Mark where platelets are.
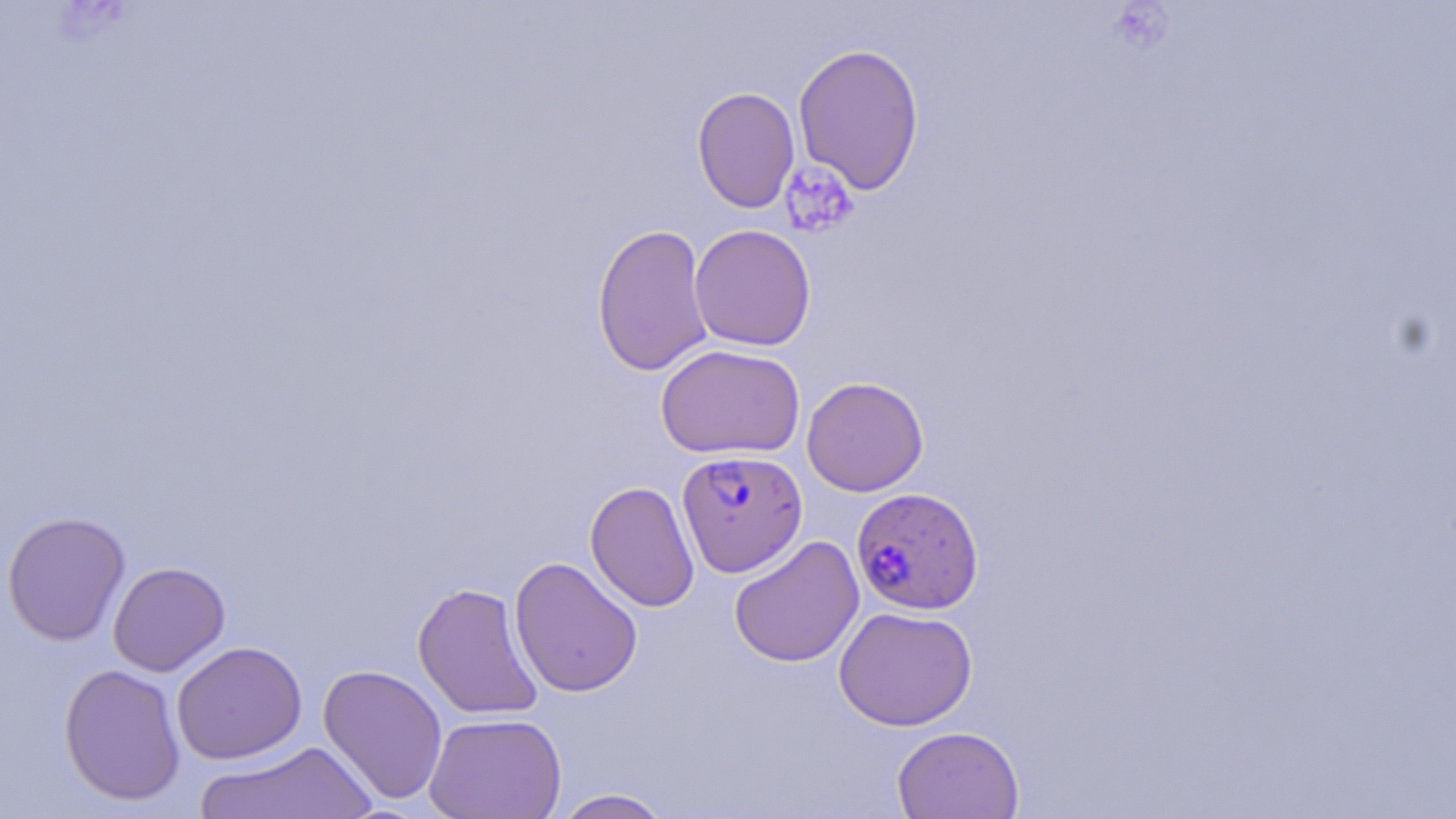

Approximate bounding boxes as (x1,y1)-(x2,y2) corner pairs in pixels.
Platelets: (780,162)-(859,239).

Uninfected red blood cell locations: (792,43)-(925,195), (692,86)-(800,214), (591,223)-(714,376), (689,224)-(816,351), (655,343)-(806,459), (801,376)-(929,496), (585,481)-(700,613), (2,511)-(131,645), (728,535)-(864,668), (509,556)-(643,698), (107,561)-(230,676), (412,582)-(544,720), (834,606)-(977,731), (171,641)-(307,765), (59,654)-(308,785), (59,663)-(186,806), (317,664)-(448,805), (424,712)-(567,819), (892,725)-(1025,819), (194,741)-(380,818), (550,788)-(675,819). Plasmodium falciparum-infected red blood cell locations: (676,449)-(806,577), (851,486)-(984,615). Slide-level diagnosis: Plasmodium falciparum. Thin blood film. 1000x magnification. Image is 1456×819 pixels. One field of a larger specimen. May-Grünwald-Giemsa-stained preparation. Optical microscopy.